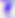
Summary:
  - Modality: micrograph
  - Identification: Toxoplasma gondii
  - Magnification: 400x